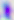
400x magnification. Micrograph. Toxoplasma gondii is seen.